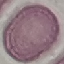

Summary:
  - Malaria status: uninfected
  - Preparation: thin blood film
  - Capture: smartphone through the microscope eyepiece
  - Image type: automatically extracted cell patch, resized to 64 × 64 pixels
  - Stain: Giemsa